Outline each blood parasite and name the species.
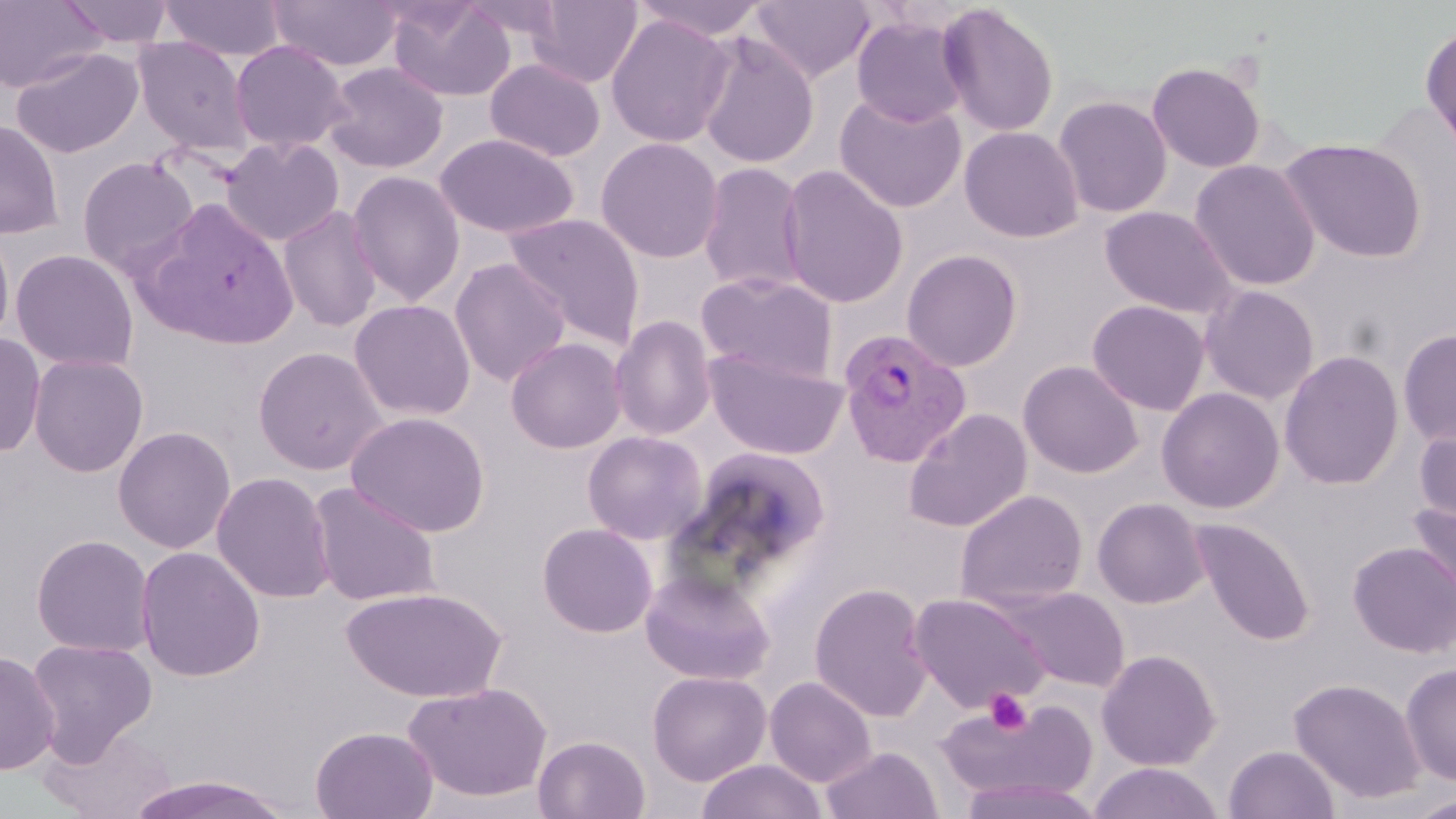
Approximate bounding boxes as [x1, y1, x2, y2] in pixels.
Plasmodium vivax-infected red blood cells: [838, 328, 972, 467].
No Plasmodium falciparum, Plasmodium ovale, Plasmodium malariae, Babesia divergens, or Trypanosoma brucei observed.

{
  "slide_level_diagnosis": "Plasmodium vivax",
  "preparation": "thin blood film",
  "uninfected_red_blood_cell_locations": "approximate bounding boxes as [x1, y1, x2, y2] in pixels: [0, 0, 106, 94], [59, 0, 176, 49], [160, 0, 286, 61], [267, 0, 401, 72], [386, 0, 517, 103], [527, 0, 642, 88], [631, 0, 773, 41], [749, 0, 875, 84], [937, 3, 1059, 138], [605, 13, 735, 148], [851, 15, 970, 127], [1420, 23, 1456, 161], [696, 33, 819, 169], [132, 36, 254, 157], [229, 40, 351, 154], [10, 46, 144, 159], [485, 58, 605, 162], [322, 61, 449, 174], [1147, 61, 1266, 173], [834, 92, 967, 213], [1053, 95, 1173, 218], [1367, 102, 1455, 232], [0, 119, 63, 239], [959, 126, 1084, 243], [434, 133, 579, 239], [220, 136, 345, 247], [596, 137, 724, 263], [1279, 138, 1426, 263], [76, 155, 199, 278], [1189, 159, 1322, 292], [697, 162, 808, 294], [778, 165, 909, 309], [346, 170, 466, 307], [136, 203, 301, 351], [278, 205, 384, 333], [1100, 206, 1237, 319], [503, 213, 645, 348], [0, 226, 16, 350], [10, 248, 139, 373], [901, 249, 1023, 372], [450, 258, 571, 387], [697, 271, 839, 385], [1199, 285, 1320, 405], [349, 299, 476, 421], [1087, 300, 1210, 415], [610, 315, 717, 441], [1397, 329, 1456, 448], [0, 332, 46, 458], [505, 337, 627, 454], [252, 345, 389, 475], [704, 350, 848, 460], [1279, 350, 1405, 490], [28, 353, 149, 477], [1017, 360, 1144, 479], [1156, 387, 1285, 513], [902, 408, 1032, 532], [345, 411, 491, 538], [1413, 421, 1456, 528], [112, 425, 236, 554], [581, 430, 708, 545], [675, 446, 831, 586], [211, 471, 336, 603], [308, 482, 442, 607], [954, 489, 1088, 610], [1092, 497, 1209, 609], [1407, 499, 1456, 610], [1191, 518, 1316, 645], [536, 522, 658, 638], [31, 533, 155, 658], [1348, 540, 1456, 657], [134, 546, 266, 682], [640, 568, 775, 685], [809, 581, 934, 722], [995, 585, 1132, 692], [340, 586, 509, 703], [907, 593, 1050, 713], [26, 638, 157, 761], [0, 649, 60, 776], [1097, 649, 1221, 771], [1400, 662, 1456, 785], [648, 670, 771, 786], [764, 675, 877, 787], [1289, 677, 1427, 804], [403, 680, 552, 804], [938, 698, 1098, 805], [310, 725, 438, 819], [42, 726, 176, 818], [533, 735, 651, 818], [1223, 744, 1340, 819], [821, 746, 942, 819], [696, 759, 826, 819], [1088, 762, 1224, 819], [124, 774, 298, 819], [958, 776, 1103, 819], [1406, 794, 1456, 819]",
  "field_of_view": "single",
  "modality": "light microscopy",
  "platelet_locations": "approximate bounding boxes as [x1, y1, x2, y2] in pixels: [984, 689, 1033, 736]",
  "stain": "May-Grünwald-Giemsa",
  "magnification": "1000x",
  "image_size": "1456×819 pixels"
}